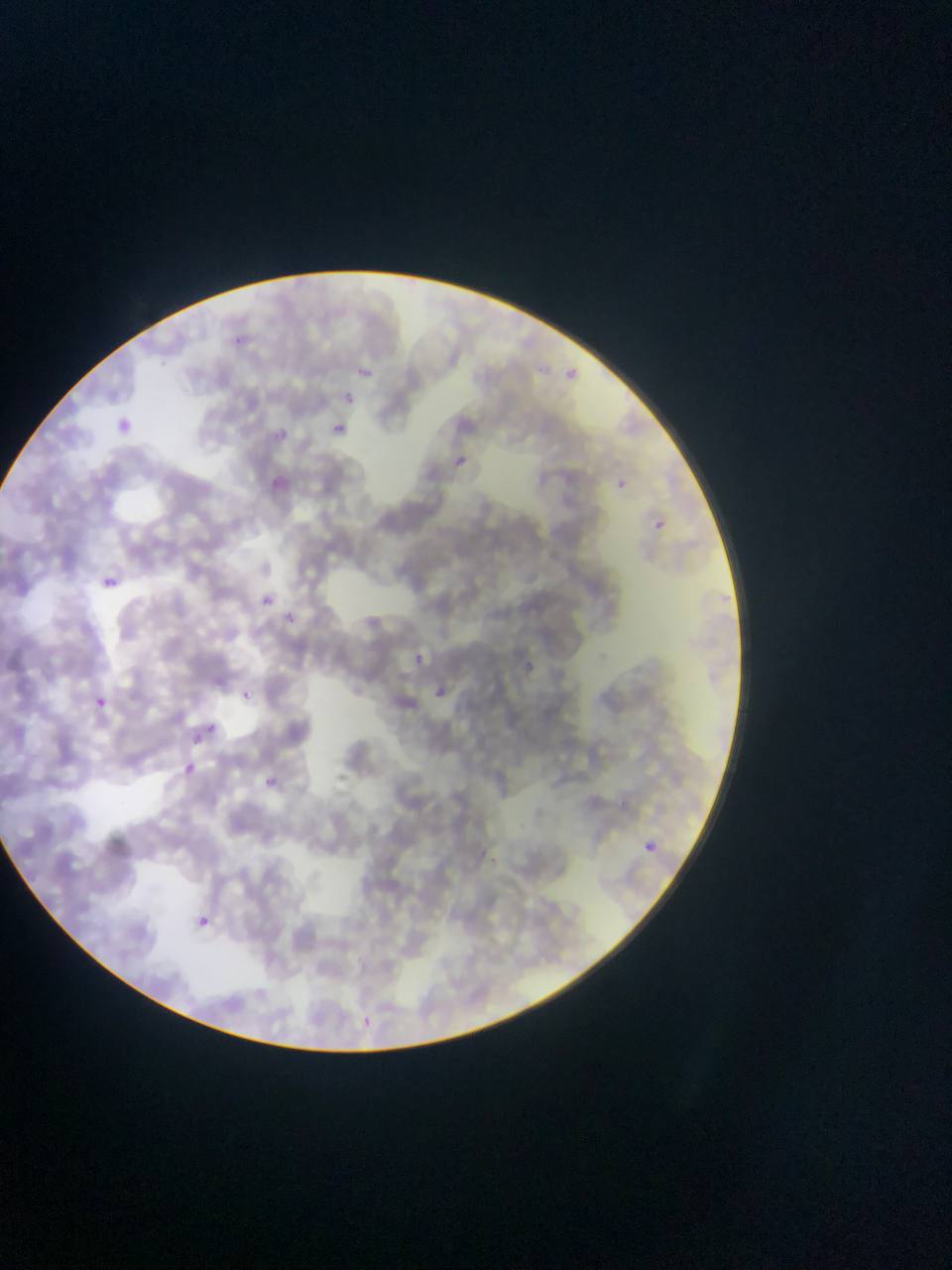

Approximate bounding boxes as [left, top, right, bottom] in pixels. Malaria parasite locations: [355, 364, 382, 380], [338, 390, 367, 408], [328, 421, 349, 439], [275, 428, 304, 449], [452, 457, 465, 469], [606, 474, 635, 495], [645, 515, 669, 538], [101, 575, 118, 590], [255, 590, 277, 611], [279, 609, 301, 629], [404, 647, 432, 672], [515, 656, 539, 680], [424, 679, 456, 709], [238, 688, 253, 702], [89, 694, 108, 712], [205, 722, 219, 735], [181, 761, 197, 777], [264, 774, 288, 791], [636, 837, 661, 859], [186, 910, 214, 936], [351, 1009, 379, 1035]. Single field of view. Image is 952×1270 pixels. Thin blood film. Photographed through a microscope with a mobile-phone camera. Collected in Ghana.